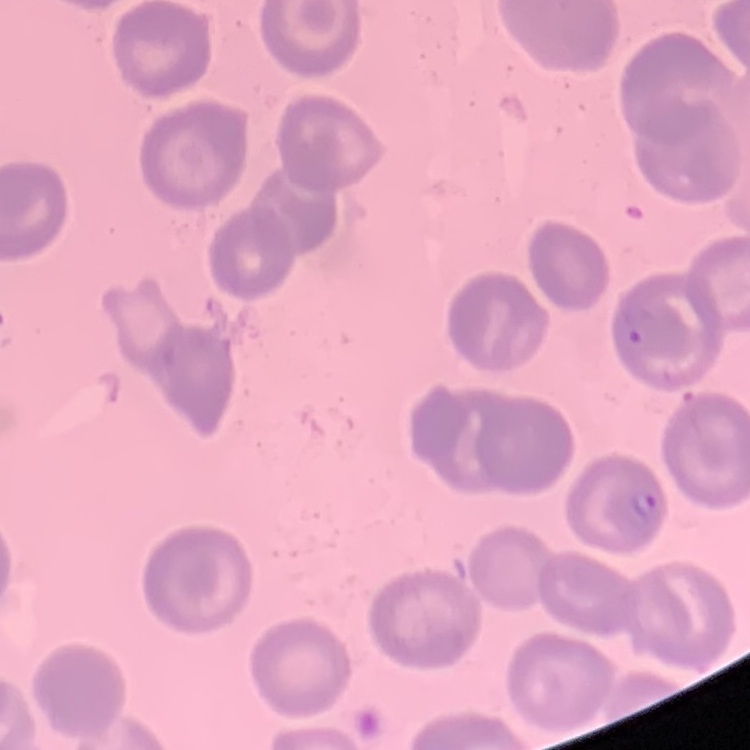

Summary:
  - Erythrocyte morphology: no rouleaux formation
  - Stain: Field's or Giemsa
  - Preparation: thin peripheral smear
  - Image type: square crop of a larger photomicrograph